Comment on the morphology of the erythrocytes.
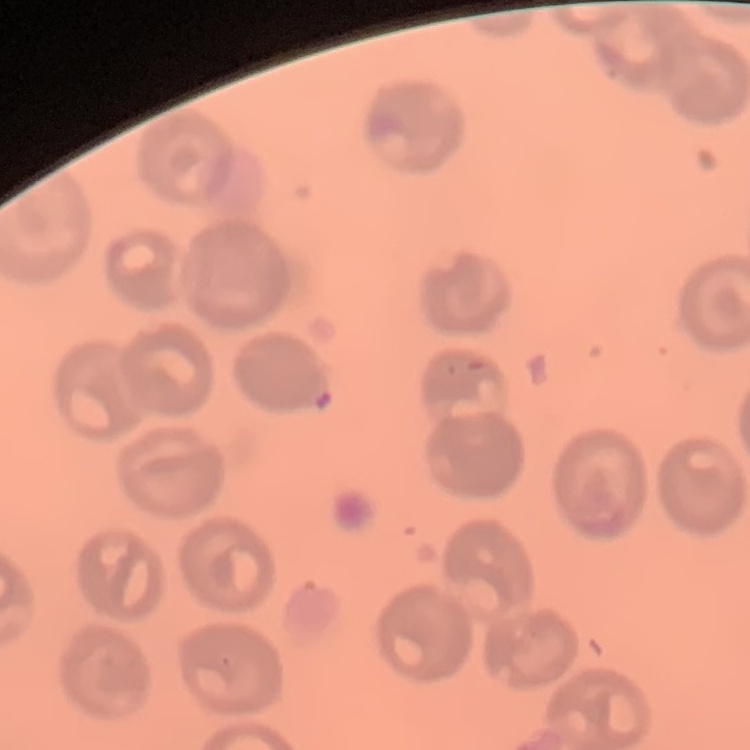

No rouleaux formation.

Thin blood film. Field's or Giemsa stain. Square crop of a larger photomicrograph.